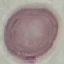
Summary:
  - Result: no malaria parasites detected
  - Image type: automatically extracted cell patch, resized to 64 × 64 pixels
  - Capture: smartphone camera at the microscope eyepiece
  - Preparation: thin blood smear
  - Stain: Giemsa